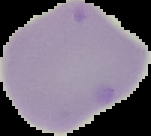
Malaria status: uninfected. The area outside the segmented cell region is set to black. Image is 151×136 pixels. From a thin blood film.